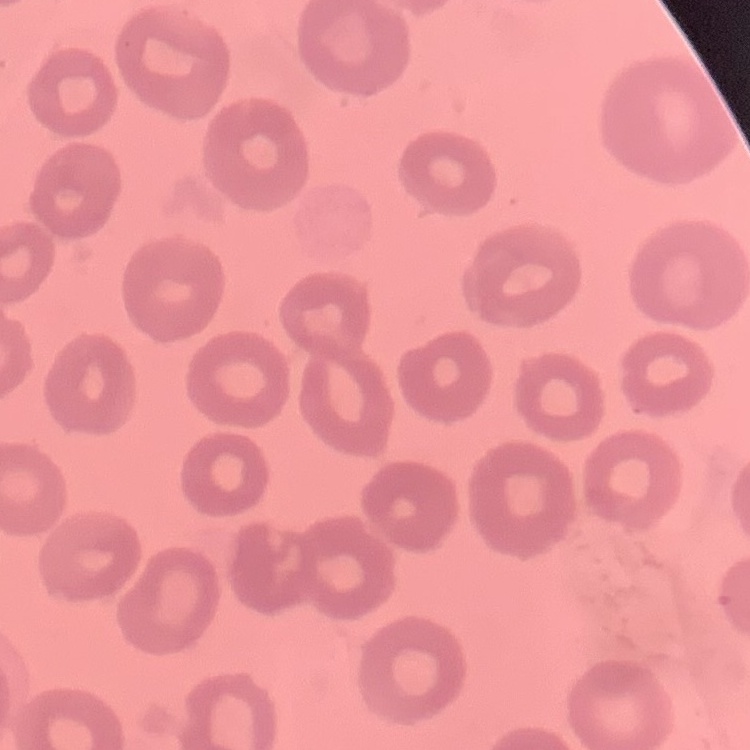 The erythrocytes show no rouleaux formation. One tile cut from a larger photomicrograph. Field's or Giemsa stain. Thin blood smear.